Outline each uninfected red blood cell.
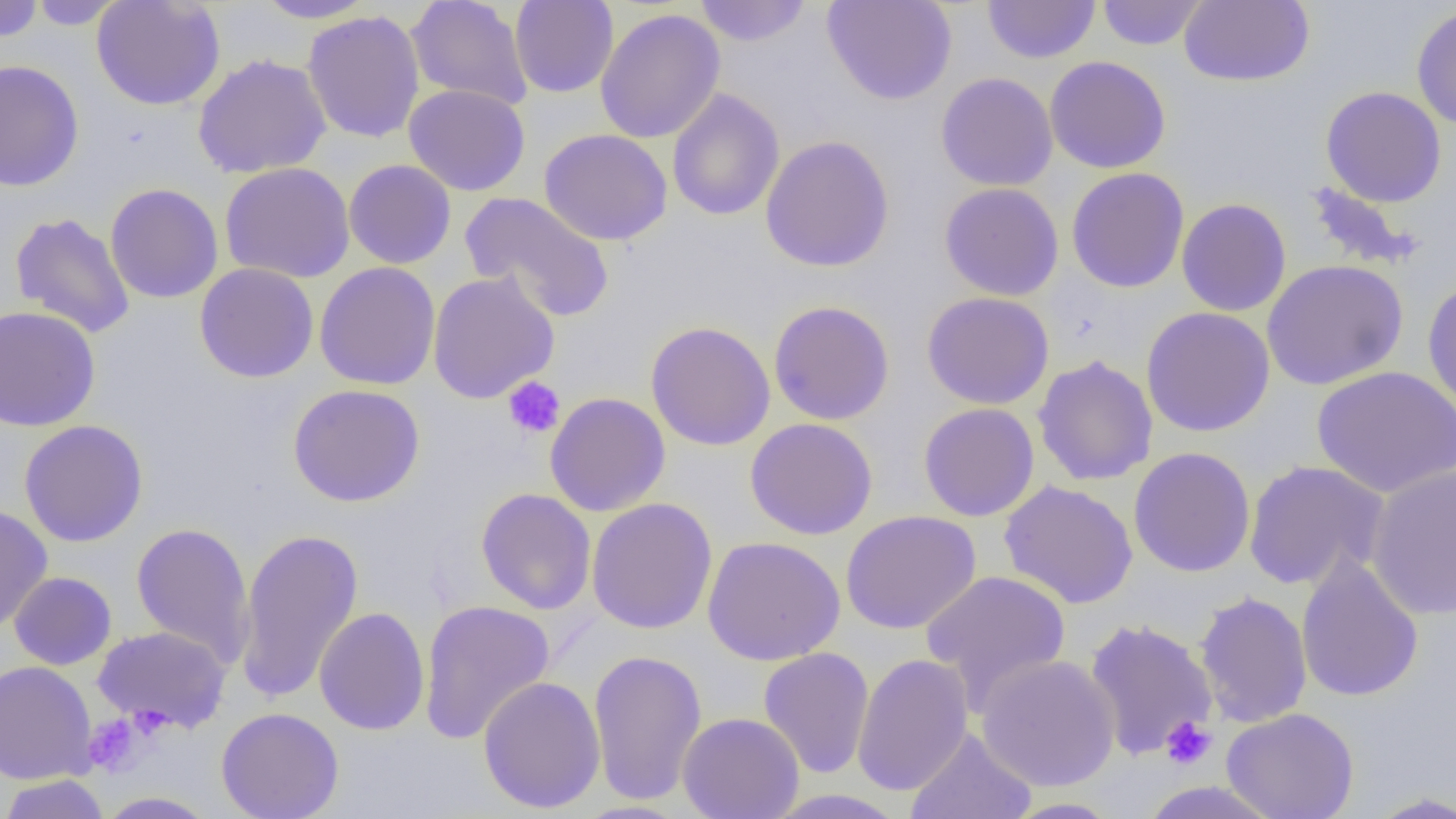
Approximate bounding boxes as (x1,y1)-(x2,y2) corner pairs in pixels.
Uninfected red blood cells: (0,0)-(44,43), (27,0)-(126,29), (92,0)-(226,111), (251,0)-(379,23), (407,0)-(533,110), (693,0)-(813,46), (822,0)-(957,105), (1097,0)-(1207,50), (1178,0)-(1314,87), (509,1)-(619,98), (982,1)-(1101,64), (1411,3)-(1456,131), (595,9)-(725,144), (302,10)-(425,143), (192,53)-(331,178), (1044,56)-(1171,173), (0,59)-(84,192), (935,72)-(1058,191), (404,84)-(531,196), (1320,86)-(1447,208), (667,89)-(785,221), (540,128)-(672,246), (760,135)-(895,272), (343,159)-(456,269), (219,162)-(355,284), (1066,167)-(1190,293), (1301,180)-(1428,272), (939,182)-(1064,301), (105,183)-(224,304), (459,191)-(615,324), (1176,197)-(1291,316), (10,212)-(135,339), (1262,260)-(1409,390), (314,262)-(441,390), (194,263)-(319,383), (427,271)-(560,404), (1422,278)-(1456,415), (922,291)-(1055,410), (768,300)-(895,425), (0,305)-(101,431), (1141,307)-(1276,437), (645,321)-(776,451), (1032,355)-(1158,486), (1312,365)-(1456,498), (287,383)-(426,507), (545,392)-(671,516), (918,403)-(1040,522), (745,417)-(878,540), (19,419)-(148,547), (1128,447)-(1256,577), (1242,460)-(1390,591), (1365,466)-(1456,620), (998,480)-(1139,609), (476,488)-(596,615), (586,497)-(718,635), (0,504)-(53,632), (840,510)-(981,635), (131,522)-(255,669), (233,527)-(364,705), (702,535)-(846,665), (1296,555)-(1424,703), (921,569)-(1072,710), (8,571)-(117,670), (1194,590)-(1312,728), (419,599)-(556,744), (314,607)-(430,735), (1082,618)-(1219,761), (92,625)-(232,734), (758,647)-(874,779), (588,649)-(708,805), (851,652)-(974,796), (975,653)-(1121,792), (0,661)-(97,784), (478,675)-(606,813), (215,707)-(344,819), (1221,707)-(1359,819), (678,712)-(805,819), (905,727)-(1037,819), (0,775)-(111,819), (763,789)-(909,819), (1363,790)-(1456,818), (96,791)-(219,818), (1001,797)-(1124,818).

Summary:
  - Platelet locations: (502,377)-(565,439), (83,713)-(146,776), (1161,716)-(1216,770)
  - Slide-level diagnosis: no evidence of blood parasites
  - Preparation: thin blood film
  - Modality: optical microscopy
  - Field of view: single
  - Magnification: 1000x
  - Image size: 1456×819 pixels